Name the parasite shown.
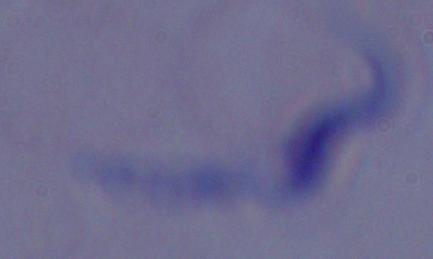

A trypanosome.

Summary:
  - Modality: photomicrograph
  - Magnification: 1000x